Give the location of every parasitized red blood cell.
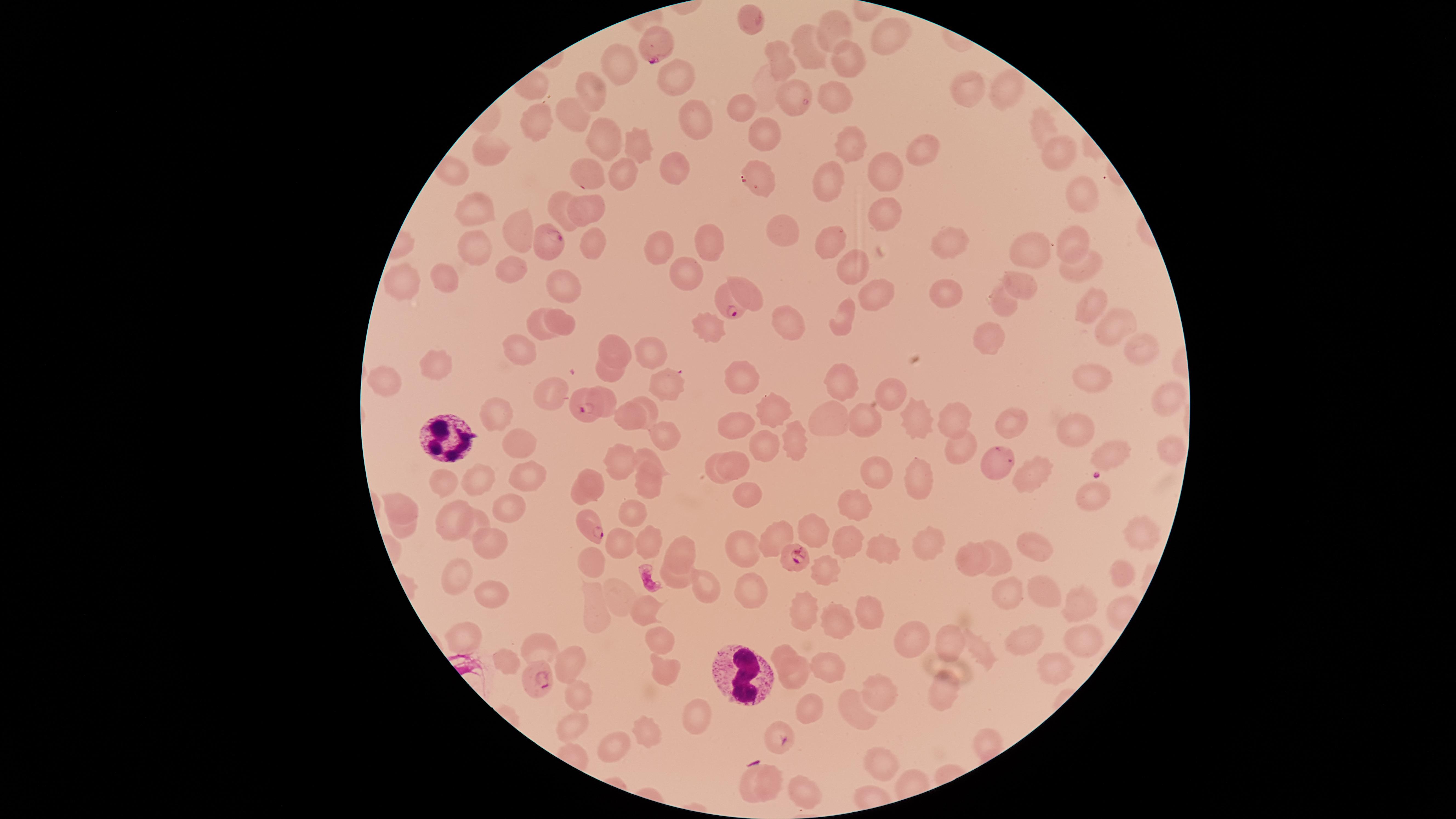

Approximate marker points as (x, y) in pixels.
Parasitized red blood cells: (652, 47), (548, 242), (725, 307), (581, 408), (999, 459), (589, 522), (793, 557), (538, 679), (783, 740).

Approximate marker points as (x, y) in pixels. White blood cells: (448, 438), (742, 677). Uninfected red blood cells: (834, 29), (886, 37), (806, 45), (778, 59), (844, 60), (621, 71), (673, 77), (1003, 85), (590, 86), (968, 90), (834, 93), (784, 96), (745, 102), (575, 110), (537, 119), (1041, 125), (694, 127), (761, 136), (602, 137), (847, 142), (636, 147), (920, 149), (1056, 151), (492, 153), (673, 166), (590, 175), (619, 175), (880, 176), (761, 180), (826, 180), (1074, 188), (558, 199), (476, 207), (589, 208), (880, 217), (784, 227), (515, 233), (824, 237), (953, 240), (1073, 240), (591, 242), (705, 245), (651, 247), (473, 249), (1028, 249), (846, 263), (1080, 266), (511, 271), (445, 280), (684, 280), (407, 285), (740, 286), (1027, 286), (561, 288), (870, 290), (951, 294), (1089, 301), (1002, 304), (848, 314), (565, 323), (1110, 323), (702, 324), (535, 325), (790, 328), (983, 338), (617, 345), (1139, 345), (519, 351), (651, 353), (435, 359), (606, 373), (384, 375), (738, 380), (1092, 380), (665, 381), (843, 384), (887, 388), (545, 395), (1171, 400), (645, 407), (772, 407), (496, 412), (628, 417), (832, 417), (864, 417), (954, 419), (917, 420), (1010, 420), (732, 426), (1074, 426), (662, 433), (518, 446), (791, 446), (760, 447), (1167, 449), (1113, 453), (622, 461), (648, 462), (737, 466), (711, 473), (879, 473), (1037, 473), (920, 476), (527, 478), (444, 480), (480, 480), (649, 486), (593, 487), (745, 490), (1090, 492), (406, 503), (852, 505), (508, 509), (630, 516), (458, 517), (477, 520), (404, 527), (807, 528), (1136, 533), (773, 538), (490, 540), (648, 540), (845, 542), (619, 546), (681, 546), (883, 546), (1034, 546), (928, 549), (744, 550), (994, 556), (594, 559), (966, 562), (825, 571), (1116, 575), (455, 579), (676, 580), (704, 587), (748, 587), (493, 590), (1041, 592), (619, 593), (1004, 596), (1078, 602), (590, 607), (804, 608), (869, 609), (641, 610), (836, 624), (469, 634), (947, 638), (663, 641), (1078, 641), (905, 645), (540, 646), (1022, 646), (781, 650), (981, 654), (506, 661), (825, 663), (1054, 663), (571, 667), (661, 674), (791, 675), (939, 690), (878, 691), (578, 697), (803, 712), (853, 713), (699, 720), (572, 729), (648, 733), (983, 734), (618, 748), (890, 764), (775, 780), (745, 783), (794, 791). Giemsa stain. Smartphone photograph through the microscope eyepiece. Image is 1456×819 pixels. Species: Plasmodium falciparum. Single field of view. Thin smear of blood. Circular visible region.